Classify this cell by malaria status.
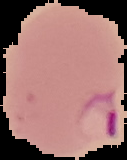

Parasitized.

Summary:
  - Preparation: thin blood smear
  - Image type: segmented cell region on a black background
  - Image size: 127×160 pixels